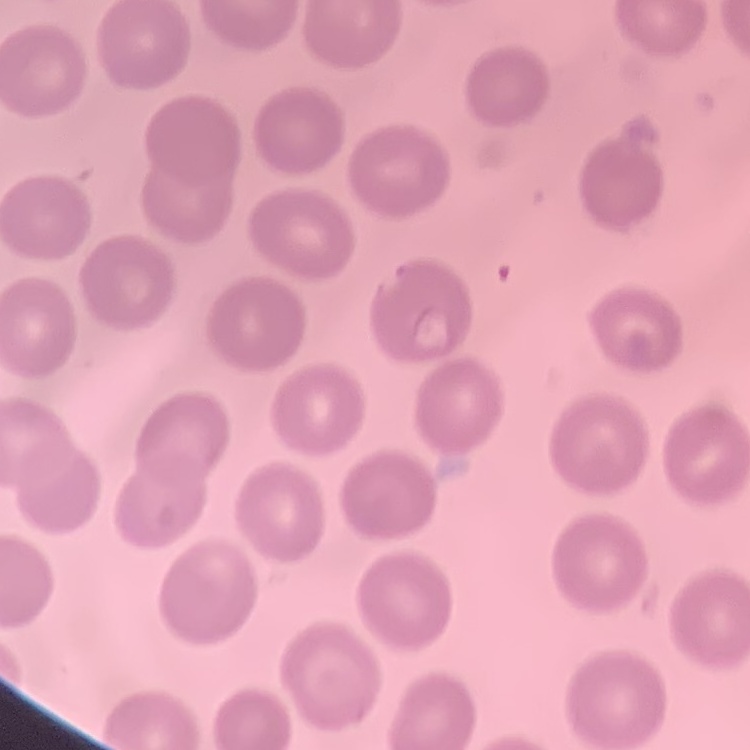

erythrocyte morphology = no rouleaux formation
stain = Field's or Giemsa
preparation = thin peripheral smear
image type = one tile cut from a larger photomicrograph